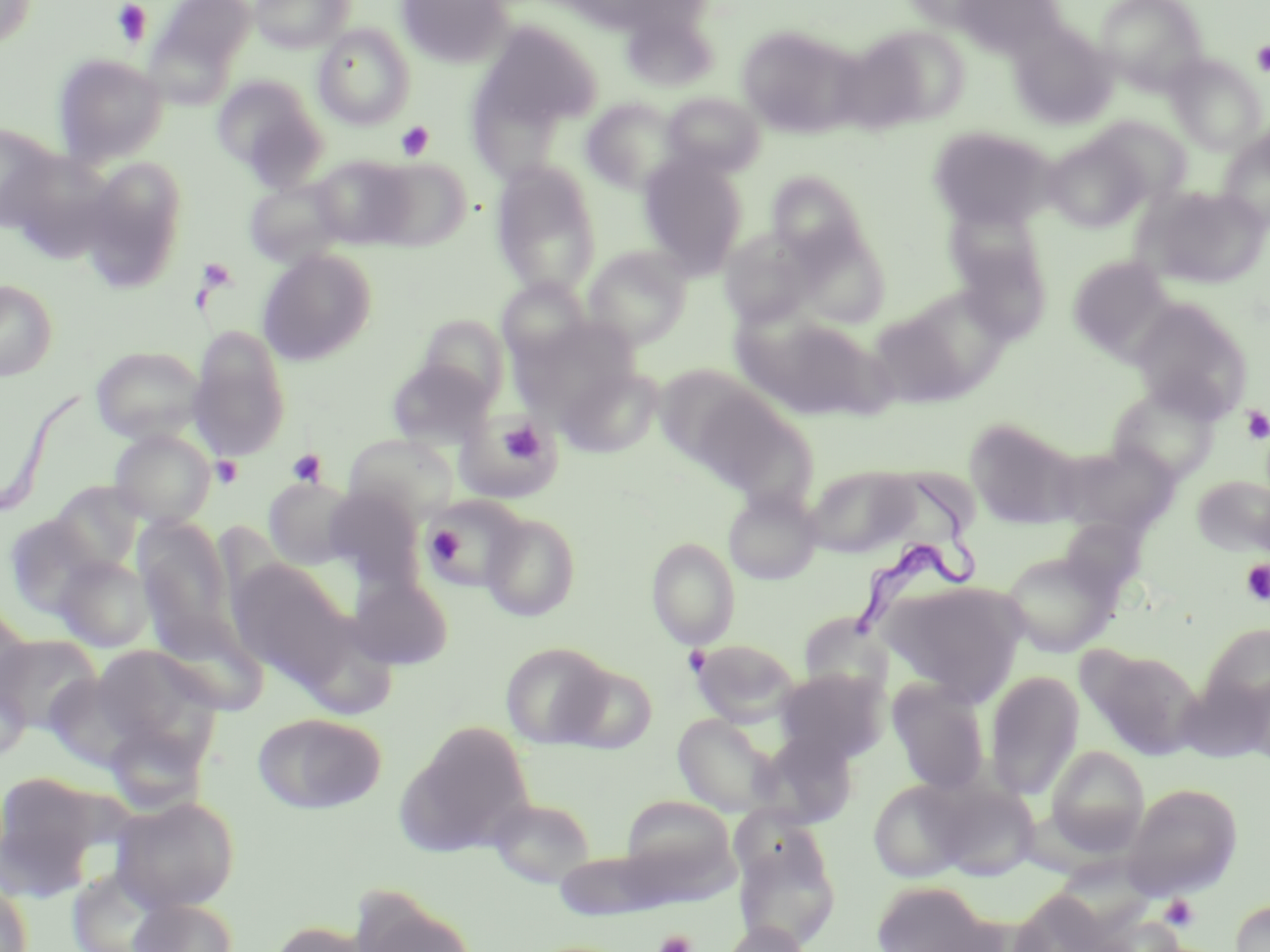

Approximate bounding boxes as named x1/y1/x2/y2 corners in pixels. Trypanosoma brucei locations: (x1=848, y1=471, x2=982, y2=639). Uninfected red blood cell locations: (x1=0, y1=0, x2=36, y2=48), (x1=154, y1=0, x2=255, y2=79), (x1=250, y1=0, x2=354, y2=53), (x1=396, y1=0, x2=513, y2=68), (x1=951, y1=0, x2=1065, y2=55), (x1=1096, y1=0, x2=1208, y2=94), (x1=620, y1=9, x2=719, y2=92), (x1=478, y1=21, x2=603, y2=131), (x1=1009, y1=23, x2=1117, y2=129), (x1=313, y1=25, x2=415, y2=129), (x1=736, y1=25, x2=861, y2=139), (x1=859, y1=25, x2=972, y2=127), (x1=53, y1=54, x2=167, y2=165), (x1=1166, y1=55, x2=1266, y2=155), (x1=212, y1=74, x2=325, y2=181), (x1=662, y1=92, x2=765, y2=178), (x1=581, y1=97, x2=684, y2=194), (x1=1089, y1=117, x2=1192, y2=207), (x1=0, y1=124, x2=62, y2=233), (x1=928, y1=125, x2=1056, y2=230), (x1=1217, y1=128, x2=1270, y2=232), (x1=1043, y1=134, x2=1151, y2=232), (x1=638, y1=153, x2=748, y2=277), (x1=310, y1=155, x2=416, y2=249), (x1=77, y1=157, x2=189, y2=290), (x1=370, y1=157, x2=471, y2=251), (x1=490, y1=161, x2=602, y2=298), (x1=767, y1=171, x2=868, y2=264), (x1=245, y1=177, x2=349, y2=267), (x1=1134, y1=185, x2=1269, y2=290), (x1=791, y1=227, x2=890, y2=328), (x1=949, y1=227, x2=1051, y2=345), (x1=719, y1=228, x2=817, y2=326), (x1=583, y1=245, x2=692, y2=348), (x1=257, y1=248, x2=377, y2=366), (x1=1067, y1=255, x2=1175, y2=363), (x1=0, y1=279, x2=57, y2=381), (x1=497, y1=279, x2=591, y2=367), (x1=888, y1=288, x2=1014, y2=398), (x1=1128, y1=297, x2=1255, y2=422), (x1=736, y1=311, x2=888, y2=421), (x1=418, y1=315, x2=511, y2=409), (x1=188, y1=324, x2=291, y2=461), (x1=91, y1=345, x2=207, y2=444), (x1=385, y1=358, x2=495, y2=450), (x1=557, y1=364, x2=664, y2=458), (x1=654, y1=364, x2=773, y2=473), (x1=679, y1=383, x2=812, y2=501), (x1=1106, y1=383, x2=1223, y2=486), (x1=455, y1=411, x2=561, y2=505), (x1=964, y1=418, x2=1080, y2=528), (x1=109, y1=429, x2=216, y2=528), (x1=344, y1=432, x2=462, y2=523), (x1=1057, y1=441, x2=1181, y2=538), (x1=805, y1=464, x2=917, y2=557), (x1=1191, y1=473, x2=1270, y2=557), (x1=263, y1=476, x2=363, y2=570), (x1=50, y1=481, x2=144, y2=575), (x1=723, y1=489, x2=821, y2=584), (x1=421, y1=495, x2=529, y2=592), (x1=480, y1=512, x2=581, y2=621), (x1=3, y1=513, x2=106, y2=618), (x1=1056, y1=516, x2=1149, y2=600), (x1=134, y1=517, x2=236, y2=646), (x1=646, y1=537, x2=741, y2=648), (x1=999, y1=547, x2=1122, y2=657), (x1=52, y1=554, x2=155, y2=652), (x1=226, y1=558, x2=354, y2=684), (x1=348, y1=571, x2=454, y2=671), (x1=882, y1=580, x2=1027, y2=701), (x1=0, y1=603, x2=33, y2=706), (x1=145, y1=612, x2=271, y2=716), (x1=1195, y1=620, x2=1270, y2=730), (x1=0, y1=633, x2=102, y2=734), (x1=690, y1=638, x2=802, y2=728), (x1=501, y1=641, x2=614, y2=748), (x1=91, y1=644, x2=222, y2=752), (x1=1079, y1=644, x2=1205, y2=761), (x1=558, y1=662, x2=657, y2=753), (x1=773, y1=668, x2=887, y2=763), (x1=984, y1=670, x2=1085, y2=801), (x1=887, y1=677, x2=992, y2=795), (x1=252, y1=712, x2=387, y2=815), (x1=672, y1=712, x2=781, y2=817), (x1=400, y1=722, x2=537, y2=856), (x1=1044, y1=745, x2=1150, y2=856), (x1=0, y1=770, x2=108, y2=898), (x1=867, y1=778, x2=977, y2=883), (x1=928, y1=778, x2=1040, y2=882), (x1=1123, y1=782, x2=1243, y2=900), (x1=619, y1=795, x2=736, y2=885), (x1=110, y1=796, x2=240, y2=913), (x1=487, y1=796, x2=596, y2=889), (x1=731, y1=830, x2=841, y2=951), (x1=0, y1=880, x2=33, y2=952), (x1=871, y1=880, x2=999, y2=952), (x1=1007, y1=887, x2=1120, y2=952), (x1=127, y1=897, x2=239, y2=952), (x1=1229, y1=900, x2=1270, y2=952), (x1=356, y1=902, x2=481, y2=952), (x1=266, y1=919, x2=382, y2=952), (x1=721, y1=921, x2=812, y2=952). Platelet locations: (x1=112, y1=1, x2=152, y2=46), (x1=1251, y1=41, x2=1270, y2=76), (x1=395, y1=121, x2=434, y2=160), (x1=196, y1=258, x2=236, y2=293), (x1=1240, y1=406, x2=1270, y2=444), (x1=496, y1=419, x2=548, y2=468), (x1=286, y1=449, x2=328, y2=488), (x1=210, y1=455, x2=244, y2=489), (x1=425, y1=526, x2=465, y2=566), (x1=1239, y1=559, x2=1270, y2=606), (x1=1158, y1=894, x2=1200, y2=932), (x1=654, y1=930, x2=696, y2=952). Slide-level diagnosis: Trypanosoma brucei. 1000x magnification. Light microscopy. Image is 1270×952 pixels. One field of a larger specimen. May-Grünwald-Giemsa-stained preparation. Thin blood film.